State which cell type is depicted.
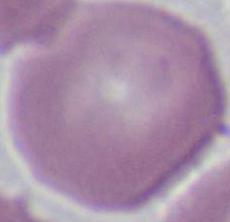
An erythrocyte.

Summary:
  - Magnification: 1000x
  - Modality: photomicrograph